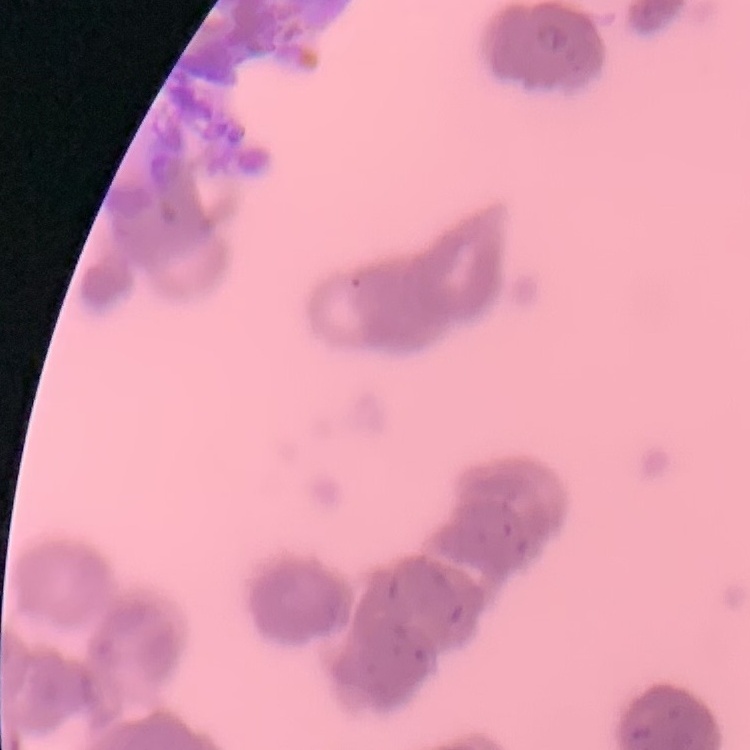
red_blood_cell_morphology: rouleaux formation
preparation: thin blood film
stain: Field's or Giemsa
image_type: square crop of a larger photomicrograph